Name the parasite shown.
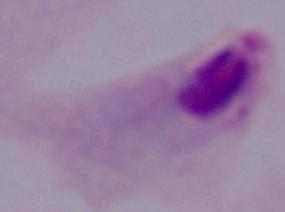

A trichomonad.

modality = photomicrograph
magnification = 1000x